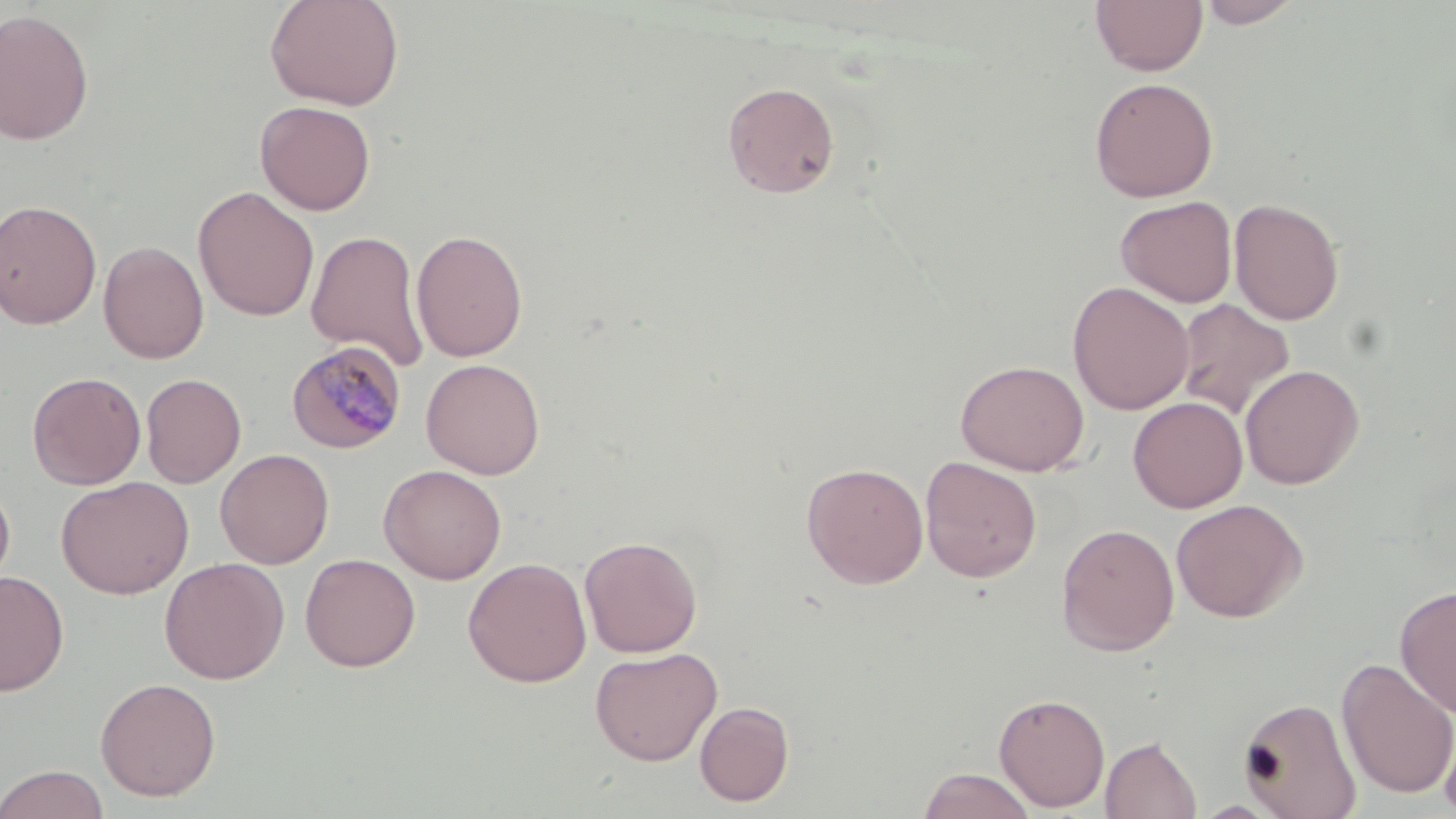
slide_level_diagnosis: Plasmodium malariae
uninfected_red_blood_cell_locations: 'approximate bounding boxes as (x1, y1, x2, y2) in pixels: (264, 0, 405, 111), (1090, 0, 1208, 76), (1196, 0, 1303, 28), (0, 8, 95, 145), (1088, 76, 1219, 202), (722, 81, 840, 198), (254, 100, 376, 215), (192, 186, 319, 321), (1115, 196, 1238, 307), (1228, 197, 1344, 325), (0, 198, 102, 330), (305, 228, 430, 370), (410, 229, 528, 362), (98, 240, 209, 363), (1068, 281, 1194, 416), (1173, 298, 1296, 420), (420, 358, 546, 479), (954, 359, 1090, 476), (1240, 364, 1364, 489), (27, 371, 146, 490), (140, 373, 246, 488), (1128, 396, 1248, 513), (215, 448, 334, 569), (920, 456, 1042, 583), (801, 461, 929, 589), (378, 464, 507, 584), (0, 476, 16, 603), (56, 476, 193, 598), (1170, 498, 1307, 622), (1056, 523, 1179, 656), (579, 534, 703, 657), (300, 553, 421, 672), (159, 557, 290, 684), (463, 557, 592, 688), (0, 571, 69, 696), (1394, 584, 1456, 718), (589, 646, 722, 766), (1336, 656, 1456, 799), (95, 677, 221, 801), (993, 692, 1110, 812), (1238, 696, 1362, 819), (694, 700, 794, 806), (1438, 716, 1456, 819), (1100, 735, 1202, 819), (0, 764, 110, 819), (916, 767, 1037, 819)'
modality: optical microscopy
stain: May-Grünwald-Giemsa
magnification: 1000x
image_size: 1456×819 pixels
preparation: thin blood film
field_of_view: single
plasmodium_malariae_infected_red_blood_cell_locations: 'approximate bounding boxes as (x1, y1, x2, y2) in pixels: (287, 341, 406, 453)'